Classify this cell by malaria status.
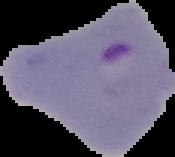
Parasitized.

Image is 175×157 pixels. From a thin blood smear. Cell region segmented out of the field of view; the surrounding area is masked to black.